Report the malaria status of this cell.
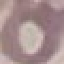

It is uninfected.

Summary:
  - Capture: smartphone through the microscope eyepiece
  - Image type: cell patch, automatically extracted from a larger field of view and resized to 64 × 64 pixels
  - Preparation: thin blood film
  - Stain: Giemsa